Outline each blood parasite and name the species.
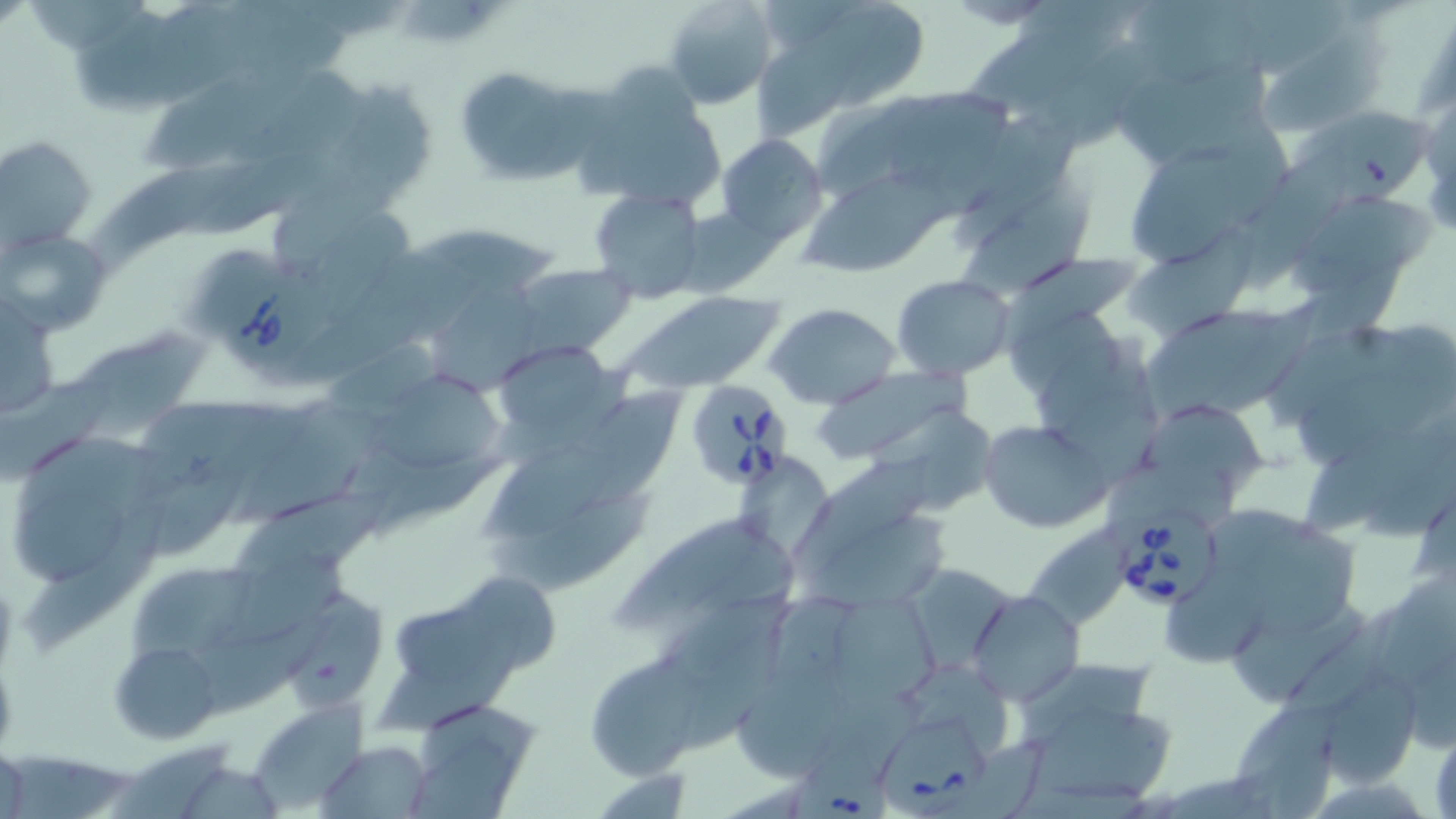

Approximate bounding boxes as (x1,y1)-(x2,y2) corner pairs in pixels.
Babesia divergens-infected red blood cells: (211,258)-(325,372), (681,379)-(797,490), (1118,503)-(1224,610), (879,716)-(986,815), (796,735)-(891,819).
No Plasmodium falciparum, Plasmodium ovale, Plasmodium malariae, Plasmodium vivax, or Trypanosoma brucei observed.

Uninfected red blood cell locations: (24,0)-(152,53), (662,0)-(779,108), (787,0)-(930,107), (1248,0)-(1347,70), (1131,1)-(1255,83), (76,6)-(187,112), (191,12)-(354,79), (963,18)-(1127,108), (1260,20)-(1385,136), (239,63)-(378,163), (1179,63)-(1266,148), (453,66)-(594,187), (139,70)-(313,178), (1117,72)-(1204,165), (574,74)-(721,217), (320,75)-(440,207), (889,89)-(1013,191), (821,99)-(923,190), (1296,111)-(1434,207), (954,114)-(1076,243), (717,133)-(829,245), (1,135)-(96,255), (1135,143)-(1240,263), (1244,143)-(1349,290), (191,150)-(325,236), (88,157)-(250,272), (274,171)-(408,275), (803,172)-(951,278), (963,176)-(1100,305), (587,185)-(709,303), (1294,193)-(1437,292), (679,206)-(781,299), (311,210)-(417,321), (1125,215)-(1261,345), (4,230)-(110,335), (420,233)-(564,293), (288,252)-(452,386), (992,255)-(1138,351), (508,262)-(633,355), (893,274)-(1016,379), (431,279)-(542,392), (619,293)-(785,394), (2,294)-(59,422), (1204,296)-(1329,420), (765,304)-(900,409), (1004,308)-(1119,400), (1144,309)-(1277,414), (1271,325)-(1421,416), (74,327)-(215,442), (1035,334)-(1154,436), (494,342)-(624,445), (1294,366)-(1427,468), (813,367)-(963,464), (365,370)-(509,482), (0,374)-(114,482), (1067,386)-(1167,477), (581,388)-(688,514), (138,397)-(282,496), (1142,402)-(1272,488), (235,403)-(389,527), (881,405)-(1000,516), (978,419)-(1110,533), (1299,431)-(1453,532), (19,433)-(167,527), (485,439)-(618,535), (345,445)-(514,535), (1364,446)-(1456,540), (792,457)-(934,577), (737,458)-(837,559), (148,461)-(263,552), (484,483)-(653,597), (234,485)-(399,573), (13,486)-(126,588), (1213,503)-(1360,633), (607,505)-(777,630), (22,507)-(164,658), (804,511)-(954,614), (1017,519)-(1139,631), (223,550)-(352,643), (128,558)-(257,655), (1360,564)-(1456,727), (909,566)-(1014,670), (1158,574)-(1264,668), (471,576)-(561,670), (669,589)-(795,672), (968,590)-(1083,706), (834,595)-(945,694), (289,597)-(389,709), (393,602)-(494,686), (1228,605)-(1363,705), (188,609)-(350,718), (683,625)-(777,750), (380,632)-(522,736), (110,640)-(219,742), (585,657)-(700,780), (1023,657)-(1158,733), (910,662)-(1014,753), (738,664)-(843,784), (1327,676)-(1421,780), (814,689)-(939,780), (248,701)-(370,807), (425,701)-(543,774), (1027,705)-(1176,802), (1239,705)-(1340,819), (404,737)-(537,819), (318,740)-(434,817), (941,742)-(1048,819), (109,744)-(233,819), (0,755)-(135,819), (185,767)-(280,819), (605,772)-(692,819). Slide-level diagnosis: Babesia divergens. Optical microscopy. Thin blood smear. Single field of view. 1000x magnification. Image is 1456×819 pixels. May-Grünwald-Giemsa stain.